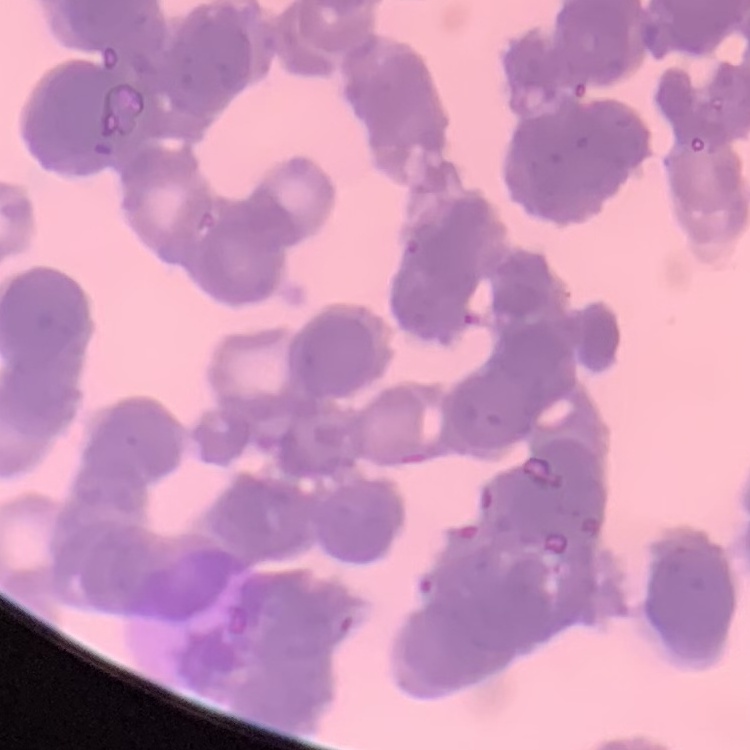
The red blood cells exhibit rouleaux formation. Field's or Giemsa stain. Thin peripheral smear. One tile cut from a larger photomicrograph.